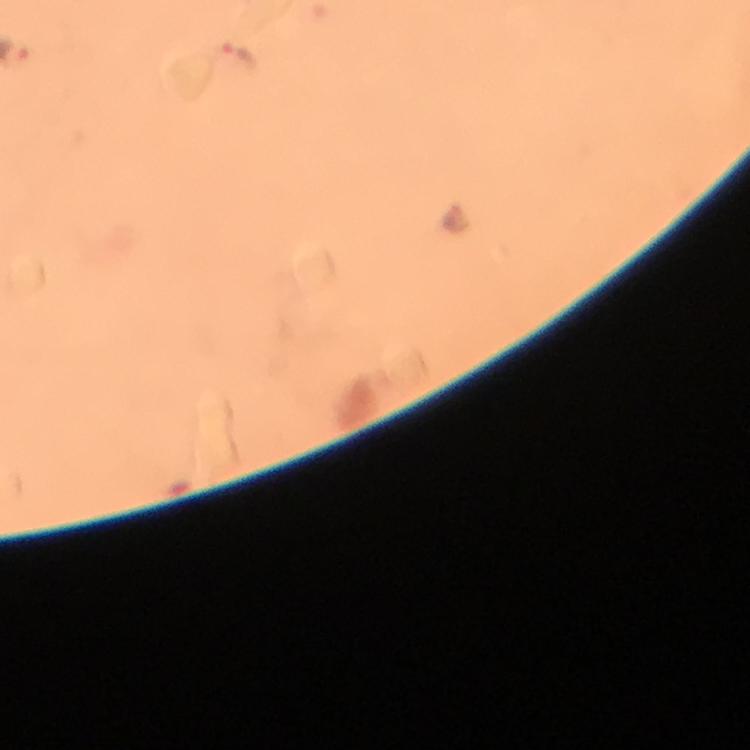
stain = Giemsa
immersion oil = applied
magnification = 100x
image size = 750×750 pixels
capture = smartphone photograph through a microscope
malaria parasite locations = approximate object centers, in pixels from the top-left corner: (x=240, y=56)
preparation = thick blood film
cropped from = one field of view
context = from a malaria diagnostic workup